Report the malaria status of this cell.
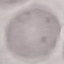
It is uninfected.

Photographed with a smartphone camera at the microscope eyepiece. Thin blood film. Giemsa stain. Cell patch, automatically extracted from a larger field of view and resized to 64 × 64 pixels.